Locate every Plasmodium parasite.
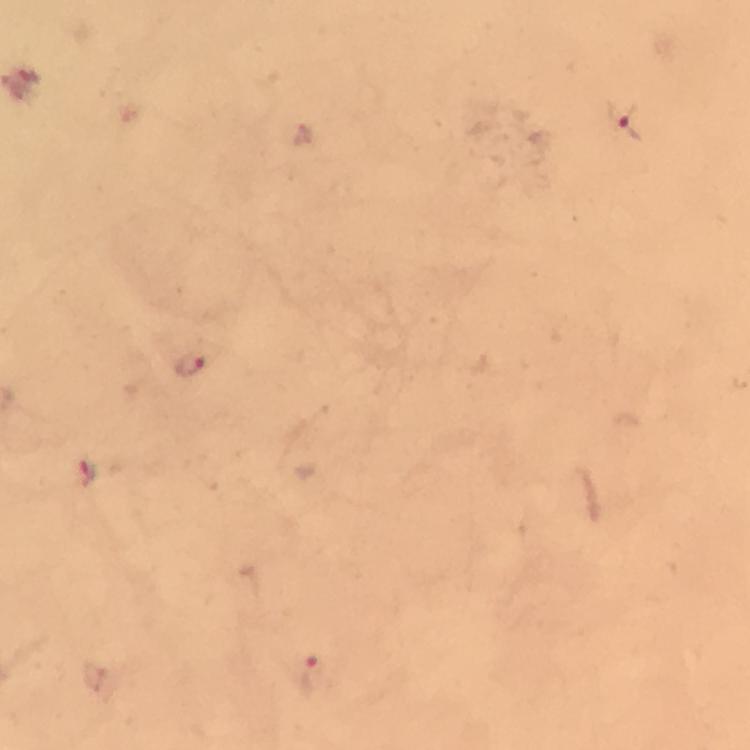

Approximate centers as {x, y} in pixels.
Plasmodium parasites: {631, 120}, {191, 363}, {87, 472}, {314, 680}.

Summary:
  - Preparation: thick smear
  - Context: from a diagnostic examination for malaria
  - Magnification: 100x
  - Immersion oil: applied
  - Stain: Giemsa
  - Image size: 750×750 pixels
  - Capture: smartphone camera through the microscope
  - Cropped from: a single field of view